Name the parasite shown.
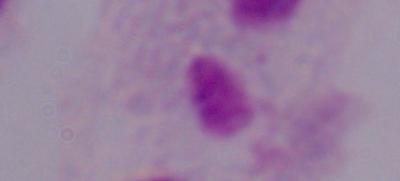

This is a trichomonad.

Summary:
  - Magnification: 1000x
  - Modality: micrograph